Assess for malaria.
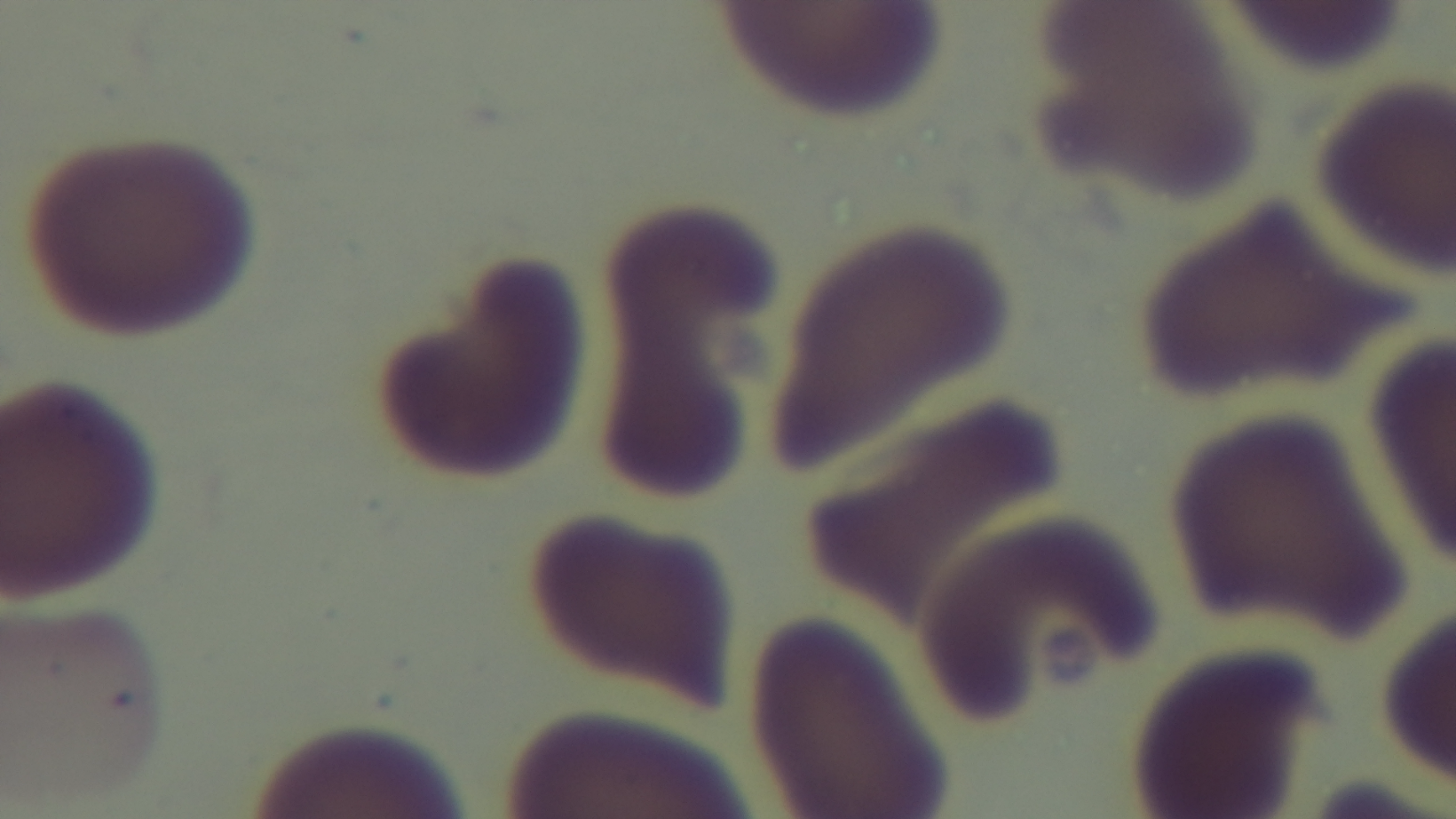
Uninfected.

objective = 100x oil immersion
stain = Giemsa
modality = light microscopy
capture = mounted 4K digital camera
field of view = single
preparation = thin blood film